Comment on the morphology of the red blood cells.
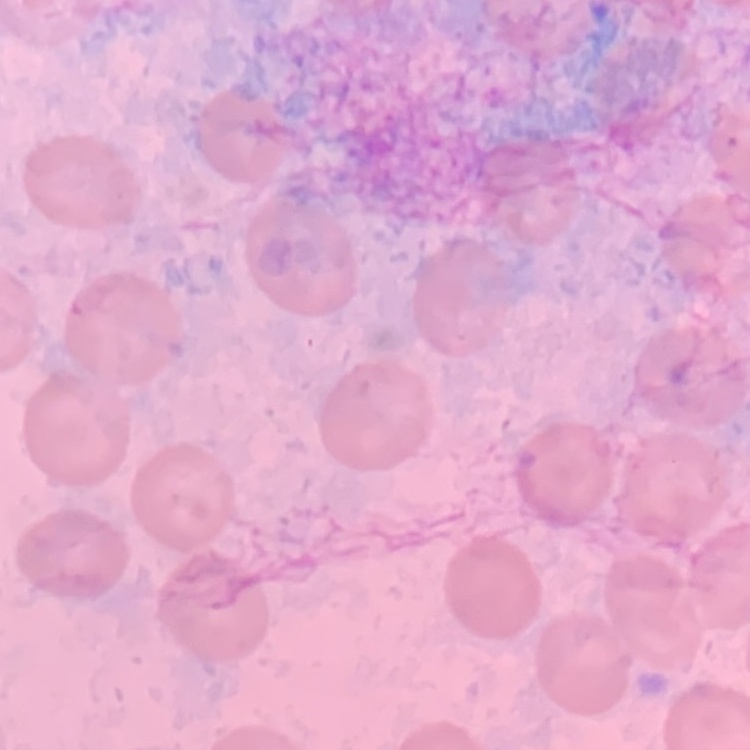
No rouleaux formation.

Square crop of a larger photomicrograph. Stained with either Field's or Giemsa. Thin blood film.